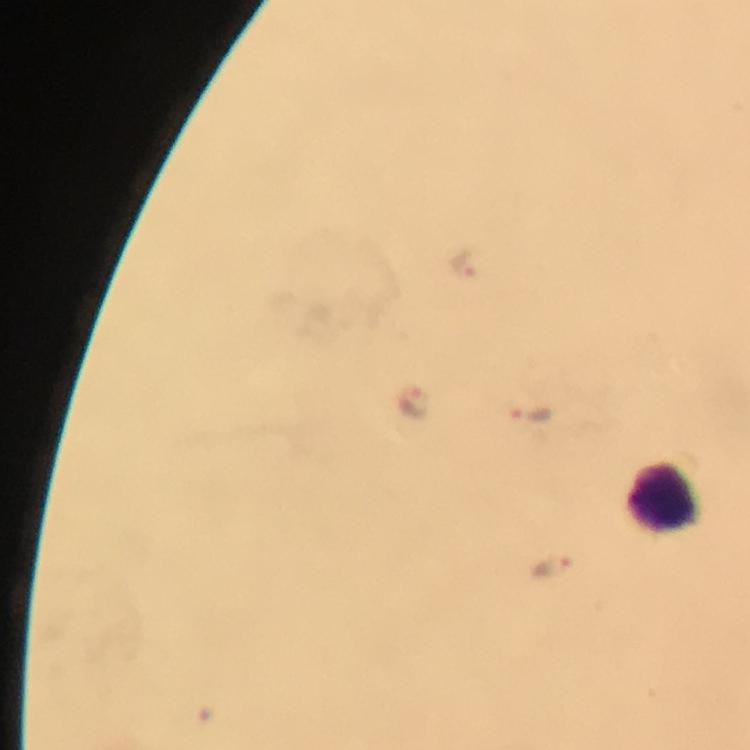

malaria parasite locations = approximate object centers, in pixels from the top-left corner: (x=465, y=261), (x=411, y=403), (x=539, y=415), (x=553, y=567)
context = from a diagnostic examination for malaria
preparation = thick smear
capture = smartphone mounted on the microscope
cropped from = one field of view
leukocyte locations = approximate object centers, in pixels from the top-left corner: (x=665, y=497)
stain = Giemsa
magnification = 100x
immersion oil = used
image size = 750×750 pixels